Classify this cell by malaria status.
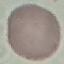

Uninfected.

Cell patch, automatically extracted from a larger field of view and resized to 64 × 64 pixels. Giemsa-stained preparation. Acquired by smartphone through the microscope eyepiece. Thin blood film.